Describe the morphology of the erythrocytes.
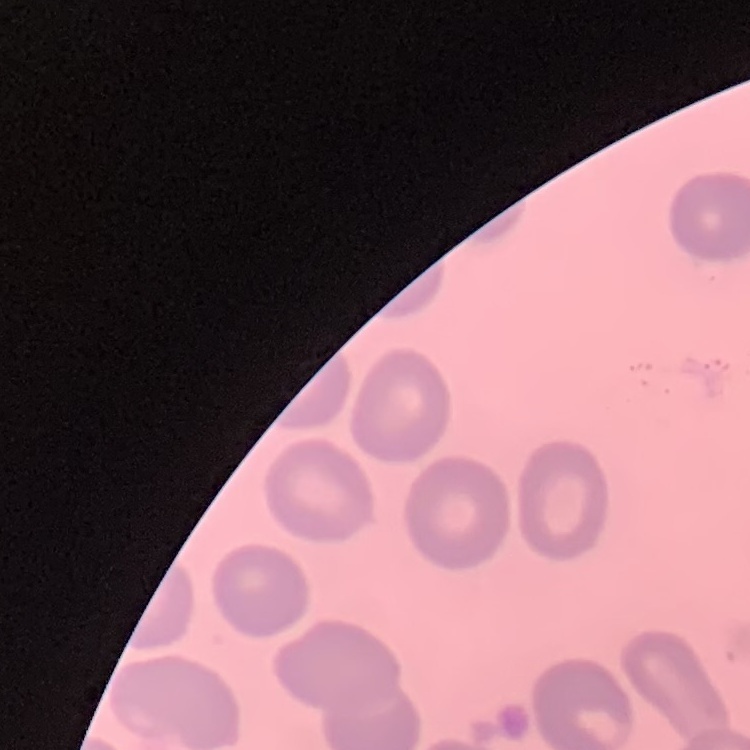

No rouleaux formation.

Square crop of a larger photomicrograph. Field's or Giemsa stain. Thin blood film.